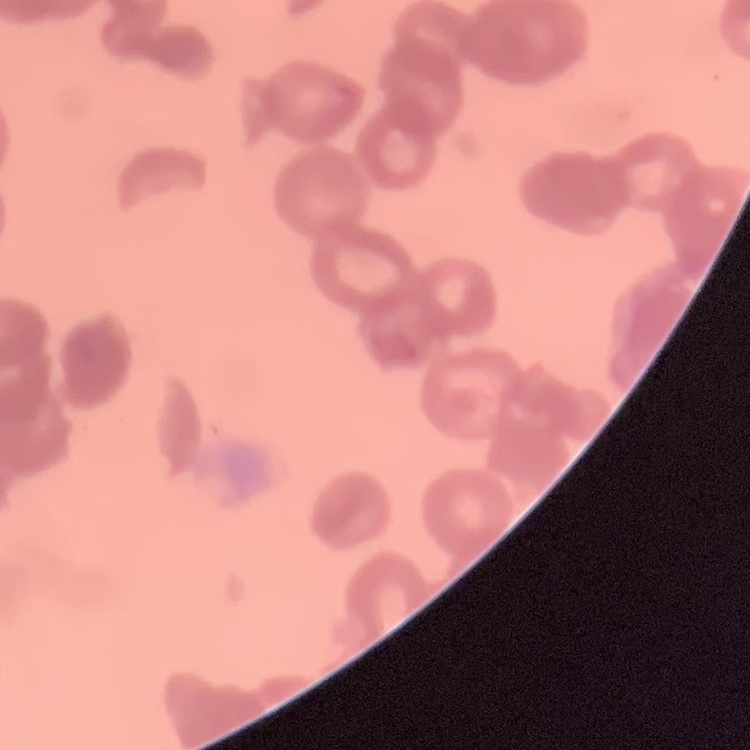

red blood cell morphology = rouleaux formation
preparation = thin blood film
image type = one tile cut from a larger photomicrograph
stain = Field's or Giemsa